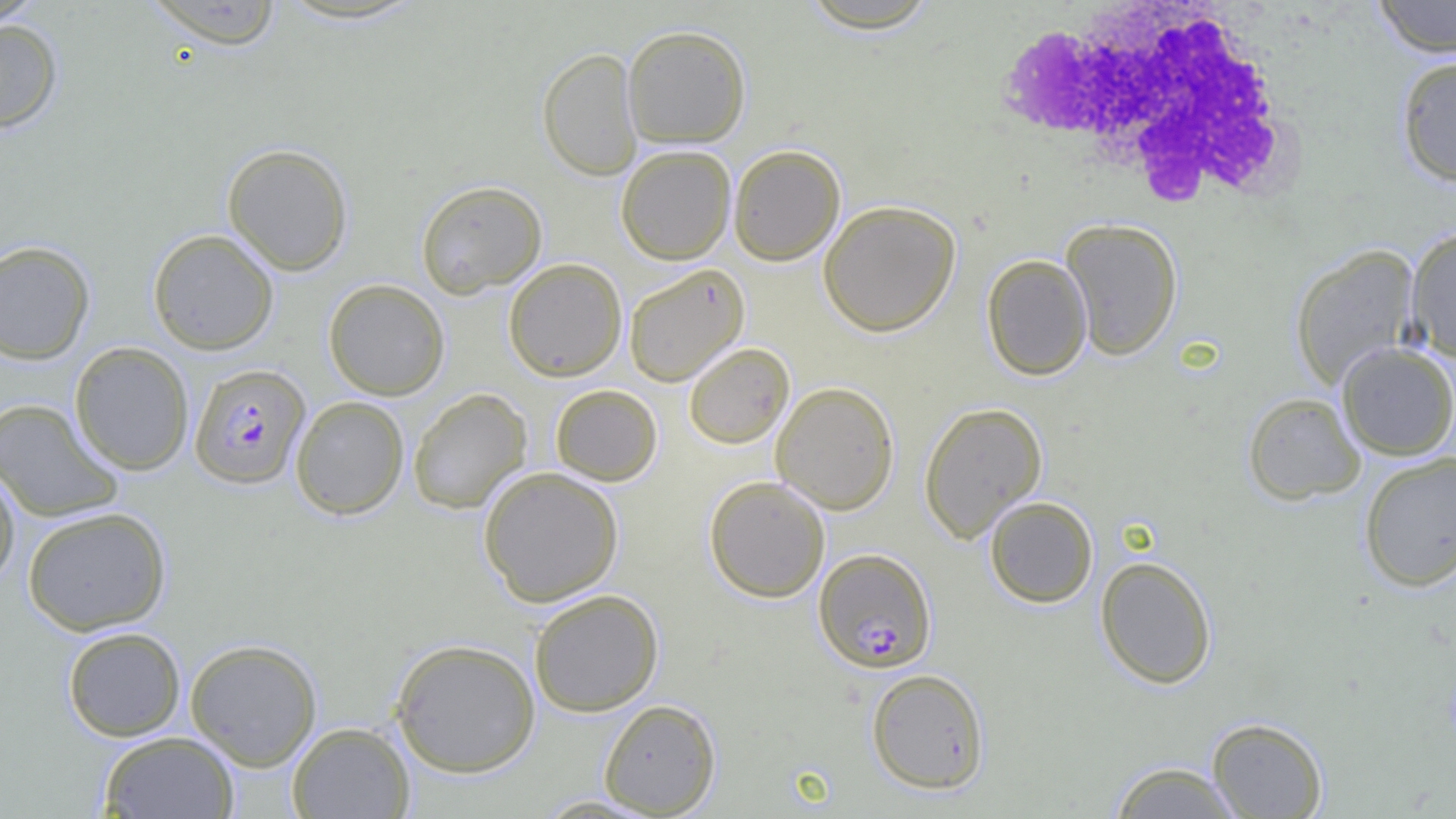
Approximate bounding boxes as named x1/y1/x2/y2 corners in pixels. White blood cell locations: (x1=994, y1=1, x2=1301, y2=210). Uninfected red blood cell locations: (x1=0, y1=0, x2=46, y2=28), (x1=796, y1=0, x2=944, y2=34), (x1=1371, y1=0, x2=1456, y2=58), (x1=142, y1=1, x2=285, y2=49), (x1=0, y1=19, x2=63, y2=133), (x1=622, y1=24, x2=752, y2=148), (x1=537, y1=47, x2=643, y2=181), (x1=1395, y1=55, x2=1456, y2=186), (x1=222, y1=143, x2=354, y2=275), (x1=616, y1=144, x2=736, y2=265), (x1=728, y1=144, x2=845, y2=265), (x1=415, y1=180, x2=547, y2=297), (x1=818, y1=200, x2=961, y2=337), (x1=1060, y1=218, x2=1183, y2=360), (x1=1405, y1=227, x2=1456, y2=362), (x1=148, y1=229, x2=279, y2=355), (x1=0, y1=240, x2=95, y2=364), (x1=1290, y1=245, x2=1421, y2=390), (x1=981, y1=254, x2=1092, y2=381), (x1=503, y1=258, x2=627, y2=381), (x1=624, y1=264, x2=750, y2=386), (x1=323, y1=279, x2=450, y2=400), (x1=69, y1=341, x2=194, y2=476), (x1=684, y1=342, x2=794, y2=448), (x1=1336, y1=342, x2=1456, y2=460), (x1=771, y1=381, x2=899, y2=515), (x1=550, y1=384, x2=662, y2=486), (x1=408, y1=388, x2=532, y2=514), (x1=1242, y1=392, x2=1366, y2=505), (x1=290, y1=395, x2=409, y2=520), (x1=0, y1=398, x2=124, y2=523), (x1=919, y1=400, x2=1047, y2=542), (x1=1358, y1=450, x2=1456, y2=592), (x1=0, y1=465, x2=21, y2=591), (x1=478, y1=466, x2=624, y2=607), (x1=704, y1=475, x2=830, y2=603), (x1=984, y1=496, x2=1098, y2=608), (x1=22, y1=507, x2=171, y2=635), (x1=1095, y1=556, x2=1217, y2=689), (x1=529, y1=589, x2=664, y2=716), (x1=62, y1=626, x2=187, y2=741), (x1=185, y1=638, x2=322, y2=771), (x1=389, y1=638, x2=541, y2=777), (x1=865, y1=668, x2=990, y2=794), (x1=598, y1=698, x2=721, y2=816), (x1=1207, y1=717, x2=1328, y2=818), (x1=286, y1=722, x2=415, y2=818), (x1=98, y1=731, x2=240, y2=819), (x1=1106, y1=760, x2=1247, y2=818). Plasmodium falciparum-infected red blood cell locations: (x1=189, y1=363, x2=311, y2=489), (x1=813, y1=548, x2=937, y2=673). Slide-level diagnosis: Plasmodium falciparum. Thin blood smear. One field of a larger specimen. Light microscopy. Image is 1456×819 pixels. 1000x magnification.